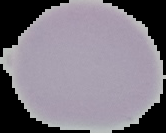
preparation: thin blood film
malaria_status: uninfected
image_size: 166×133 pixels
image_type: segmented cell region with the area outside set to black